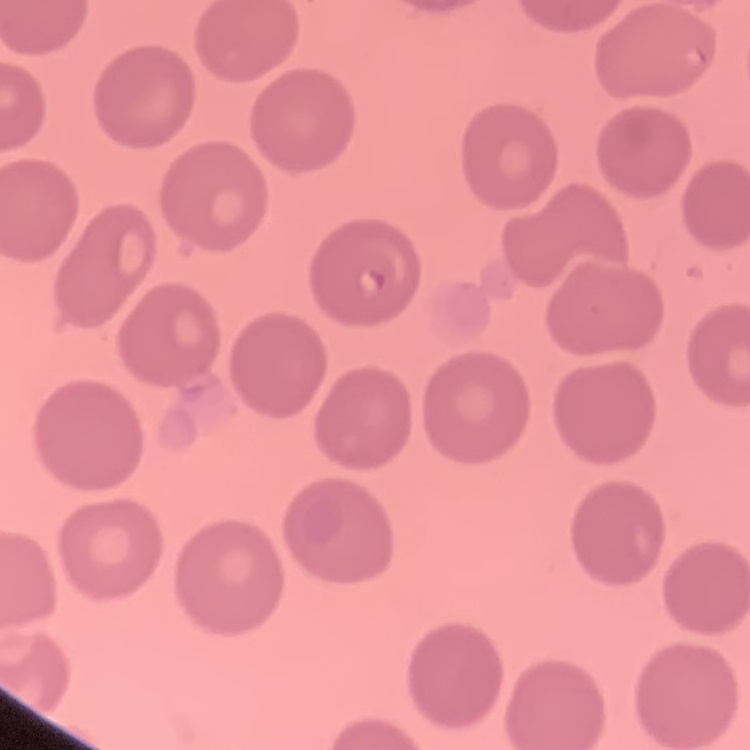

Summary:
  - Erythrocyte morphology: no rouleaux formation
  - Image type: one tile cut from a larger photomicrograph
  - Preparation: thin peripheral smear
  - Stain: Field's or Giemsa